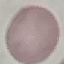

Summary:
  - Malaria status: uninfected
  - Image type: automatically extracted cell patch, resized to 64 × 64 pixels
  - Stain: Giemsa
  - Preparation: thin smear
  - Capture: smartphone camera at the microscope eyepiece